Outline each blood parasite and name the species.
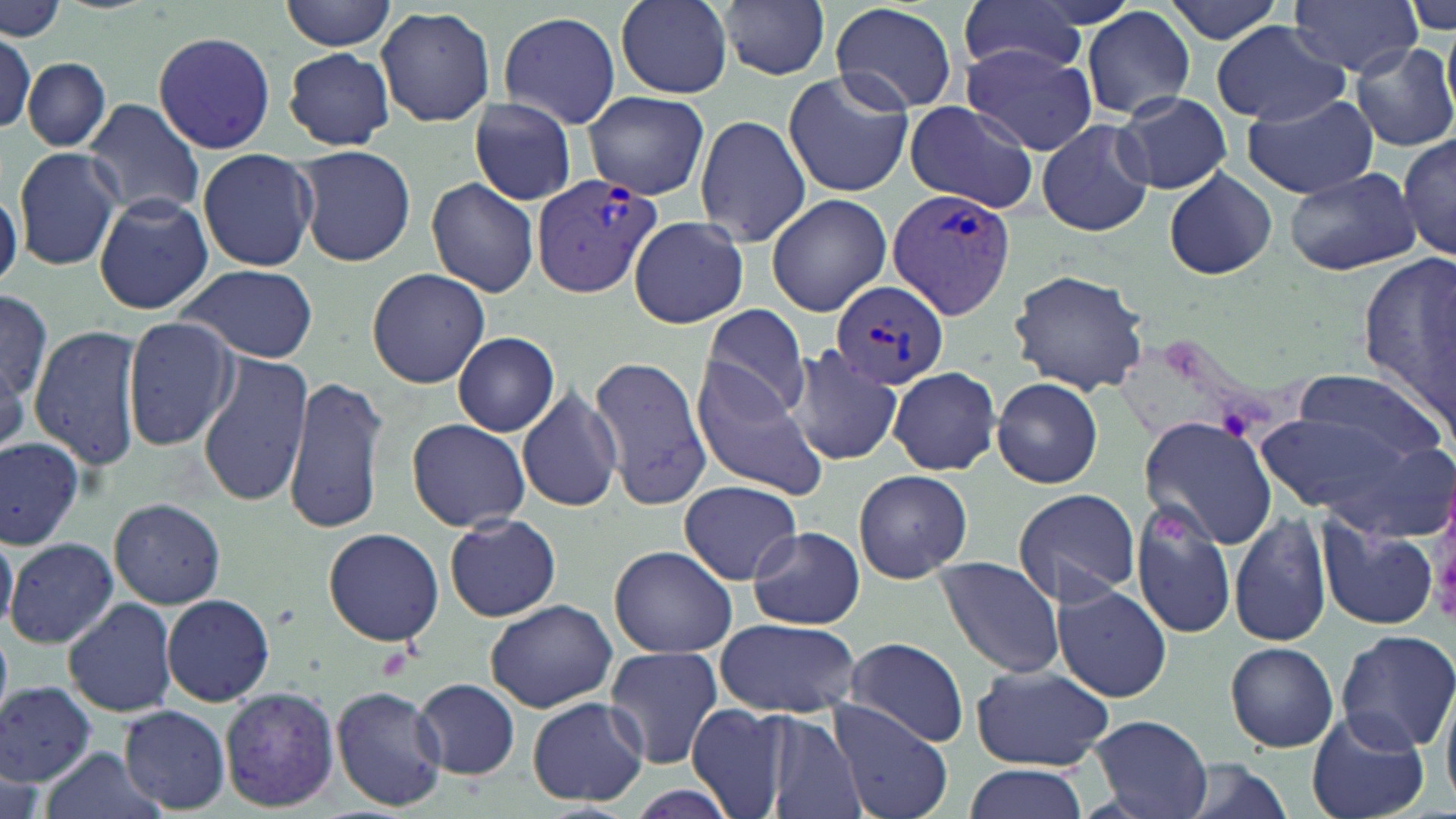
Approximate bounding boxes as [x1, y1, x2, y2] in pixels.
Plasmodium vivax-infected red blood cells: [532, 175, 663, 299], [886, 187, 1017, 320], [831, 279, 947, 388].
No Plasmodium falciparum, Plasmodium ovale, Plasmodium malariae, Babesia divergens, or Trypanosoma brucei observed.

{
  "slide_level_diagnosis": "Plasmodium vivax",
  "stain": "May-Grünwald-Giemsa",
  "magnification": "1000x",
  "image_size": "1456×819 pixels",
  "platelet_locations": "approximate bounding boxes as [x1, y1, x2, y2] in pixels: [1148, 510, 1193, 547]",
  "field_of_view": "single",
  "preparation": "thin blood smear",
  "modality": "light microscopy",
  "uninfected_red_blood_cell_locations": "approximate bounding boxes as [x1, y1, x2, y2] in pixels: [0, 0, 67, 41], [280, 0, 395, 51], [616, 0, 731, 98], [958, 0, 1090, 79], [1166, 0, 1282, 44], [1288, 0, 1421, 77], [1403, 1, 1456, 34], [717, 2, 830, 80], [830, 3, 958, 115], [377, 6, 495, 128], [1082, 7, 1194, 122], [498, 11, 620, 128], [1442, 20, 1456, 118], [1210, 21, 1351, 128], [1, 31, 36, 135], [152, 31, 276, 155], [962, 42, 1096, 155], [1350, 42, 1456, 154], [283, 48, 394, 151], [22, 58, 110, 151], [783, 71, 914, 198], [582, 91, 709, 199], [1242, 92, 1379, 201], [1115, 94, 1232, 193], [80, 99, 205, 222], [469, 100, 576, 205], [905, 100, 1039, 213], [695, 114, 811, 248], [1037, 120, 1155, 238], [1397, 133, 1456, 262], [297, 146, 416, 266], [13, 147, 122, 269], [197, 149, 318, 272], [1164, 168, 1277, 281], [1285, 168, 1420, 276], [425, 177, 539, 297], [0, 190, 24, 294], [93, 194, 213, 315], [766, 194, 890, 317], [628, 216, 748, 329], [1356, 250, 1456, 424], [179, 266, 320, 362], [367, 267, 491, 388], [1007, 269, 1152, 396], [0, 290, 50, 400], [699, 304, 811, 422], [121, 317, 237, 452], [30, 326, 142, 473], [452, 333, 559, 437], [787, 347, 902, 466], [197, 352, 313, 508], [0, 354, 28, 462], [587, 356, 713, 510], [691, 362, 828, 502], [1290, 367, 1444, 468], [888, 368, 999, 476], [284, 376, 388, 536], [992, 378, 1104, 488], [517, 389, 622, 513], [1254, 405, 1438, 525], [1138, 415, 1280, 552], [406, 419, 530, 533], [0, 437, 83, 550], [853, 469, 973, 585], [679, 481, 802, 584], [1013, 489, 1142, 607], [108, 498, 225, 609], [1130, 501, 1236, 640], [1229, 513, 1332, 649], [445, 514, 562, 621], [1316, 514, 1439, 632], [0, 525, 17, 636], [749, 526, 865, 631], [322, 528, 446, 647], [6, 537, 119, 650], [610, 545, 737, 657], [937, 558, 1065, 678], [1052, 581, 1172, 704], [162, 594, 275, 706], [63, 599, 176, 718], [485, 600, 618, 714], [714, 618, 861, 717], [0, 621, 11, 734], [1335, 630, 1456, 754], [843, 638, 968, 748], [1224, 640, 1339, 753], [605, 646, 723, 769], [970, 664, 1113, 771], [411, 678, 521, 780], [0, 681, 96, 787], [1439, 682, 1456, 819], [330, 684, 447, 812], [220, 687, 339, 811], [526, 698, 650, 805], [828, 700, 954, 819], [686, 703, 789, 818], [118, 706, 230, 813], [1306, 708, 1431, 819], [761, 711, 867, 818], [1089, 714, 1214, 819], [37, 746, 164, 819], [1, 751, 45, 819], [1176, 757, 1294, 819], [963, 763, 1089, 819]"
}